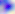
400x magnification. Toxoplasma gondii is seen. Photomicrograph.